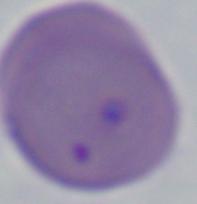

Captured at 1000x magnification. Micrograph. A Babesia parasite is seen.